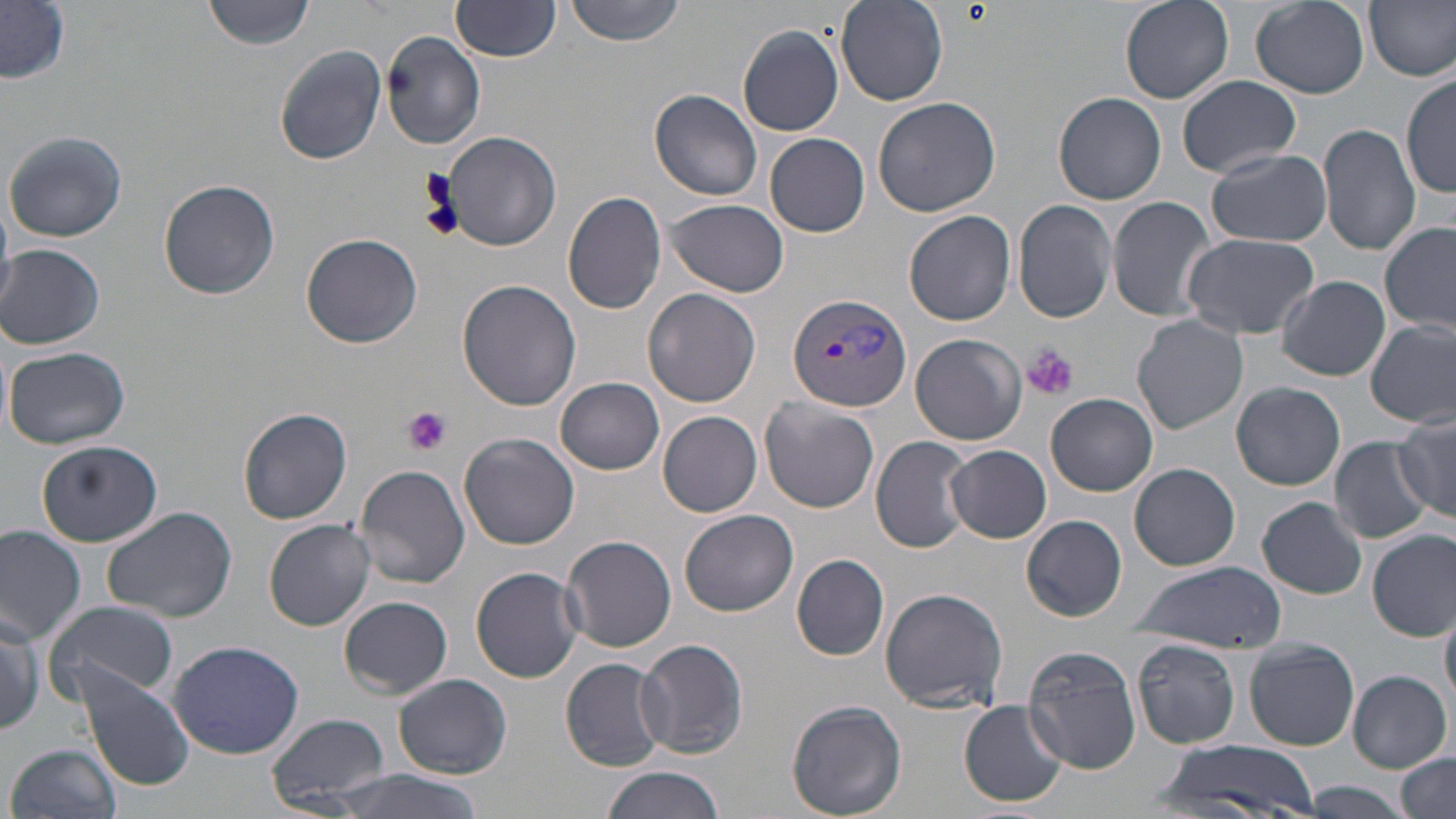
{
  "slide_level_diagnosis": "Plasmodium vivax",
  "stain": "May-Grünwald-Giemsa",
  "modality": "light microscopy",
  "uninfected_red_blood_cell_locations": "approximate bounding boxes as named x1/y1/x2/y2 corners in pixels: (x1=201, y1=0, x2=321, y2=51), (x1=451, y1=0, x2=562, y2=62), (x1=562, y1=0, x2=692, y2=46), (x1=1118, y1=0, x2=1233, y2=104), (x1=1367, y1=0, x2=1456, y2=82), (x1=835, y1=1, x2=949, y2=107), (x1=1248, y1=1, x2=1370, y2=98), (x1=1, y1=3, x2=71, y2=83), (x1=739, y1=26, x2=845, y2=136), (x1=381, y1=31, x2=485, y2=150), (x1=274, y1=44, x2=387, y2=165), (x1=1402, y1=73, x2=1456, y2=198), (x1=1175, y1=75, x2=1304, y2=179), (x1=649, y1=89, x2=763, y2=202), (x1=1053, y1=91, x2=1167, y2=205), (x1=872, y1=97, x2=1002, y2=218), (x1=1318, y1=123, x2=1420, y2=255), (x1=5, y1=129, x2=128, y2=244), (x1=440, y1=131, x2=561, y2=253), (x1=765, y1=133, x2=870, y2=237), (x1=1207, y1=148, x2=1332, y2=247), (x1=159, y1=180, x2=281, y2=300), (x1=562, y1=191, x2=667, y2=314), (x1=1106, y1=196, x2=1214, y2=322), (x1=666, y1=199, x2=789, y2=298), (x1=1013, y1=199, x2=1117, y2=322), (x1=904, y1=211, x2=1017, y2=325), (x1=1381, y1=221, x2=1455, y2=336), (x1=300, y1=233, x2=422, y2=349), (x1=1182, y1=233, x2=1318, y2=340), (x1=1, y1=244, x2=105, y2=350), (x1=1278, y1=276, x2=1390, y2=380), (x1=456, y1=279, x2=581, y2=411), (x1=642, y1=288, x2=762, y2=407), (x1=1132, y1=314, x2=1248, y2=435), (x1=1367, y1=321, x2=1455, y2=428), (x1=911, y1=333, x2=1026, y2=445), (x1=5, y1=346, x2=130, y2=450), (x1=555, y1=375, x2=665, y2=474), (x1=1230, y1=382, x2=1346, y2=491), (x1=1044, y1=393, x2=1159, y2=497), (x1=759, y1=397, x2=881, y2=513), (x1=238, y1=407, x2=353, y2=523), (x1=658, y1=411, x2=761, y2=517), (x1=1393, y1=414, x2=1455, y2=522), (x1=458, y1=433, x2=580, y2=550), (x1=870, y1=436, x2=973, y2=553), (x1=1328, y1=438, x2=1432, y2=543), (x1=37, y1=439, x2=163, y2=547), (x1=946, y1=443, x2=1051, y2=543), (x1=354, y1=463, x2=471, y2=588), (x1=1130, y1=464, x2=1241, y2=571), (x1=1256, y1=495, x2=1369, y2=599), (x1=102, y1=506, x2=237, y2=623), (x1=679, y1=510, x2=798, y2=617), (x1=1022, y1=514, x2=1127, y2=621), (x1=264, y1=519, x2=376, y2=630), (x1=0, y1=523, x2=88, y2=644), (x1=1368, y1=530, x2=1455, y2=640), (x1=559, y1=535, x2=678, y2=653), (x1=792, y1=553, x2=890, y2=659), (x1=1133, y1=562, x2=1285, y2=653), (x1=470, y1=567, x2=584, y2=682), (x1=879, y1=586, x2=1008, y2=714), (x1=340, y1=596, x2=452, y2=698), (x1=46, y1=599, x2=179, y2=703), (x1=1441, y1=603, x2=1456, y2=710), (x1=0, y1=608, x2=45, y2=737), (x1=634, y1=638, x2=749, y2=760), (x1=1131, y1=638, x2=1242, y2=749), (x1=1244, y1=639, x2=1359, y2=750), (x1=167, y1=641, x2=305, y2=758), (x1=1024, y1=646, x2=1140, y2=773), (x1=561, y1=656, x2=666, y2=771), (x1=1349, y1=671, x2=1450, y2=770), (x1=81, y1=672, x2=195, y2=791), (x1=394, y1=674, x2=511, y2=778), (x1=786, y1=700, x2=908, y2=818), (x1=958, y1=700, x2=1068, y2=807), (x1=266, y1=711, x2=390, y2=809), (x1=1156, y1=740, x2=1323, y2=816), (x1=8, y1=741, x2=123, y2=819), (x1=1394, y1=753, x2=1454, y2=819), (x1=599, y1=764, x2=729, y2=819), (x1=331, y1=769, x2=487, y2=819), (x1=1298, y1=783, x2=1414, y2=818)",
  "preparation": "thin blood smear",
  "platelet_locations": "approximate bounding boxes as named x1/y1/x2/y2 corners in pixels: (x1=1023, y1=344, x2=1078, y2=400), (x1=400, y1=405, x2=452, y2=456)",
  "plasmodium_vivax_infected_red_blood_cell_locations": "approximate bounding boxes as named x1/y1/x2/y2 corners in pixels: (x1=787, y1=291, x2=913, y2=412)",
  "magnification": "1000x",
  "field_of_view": "single",
  "image_size": "1456×819 pixels"
}